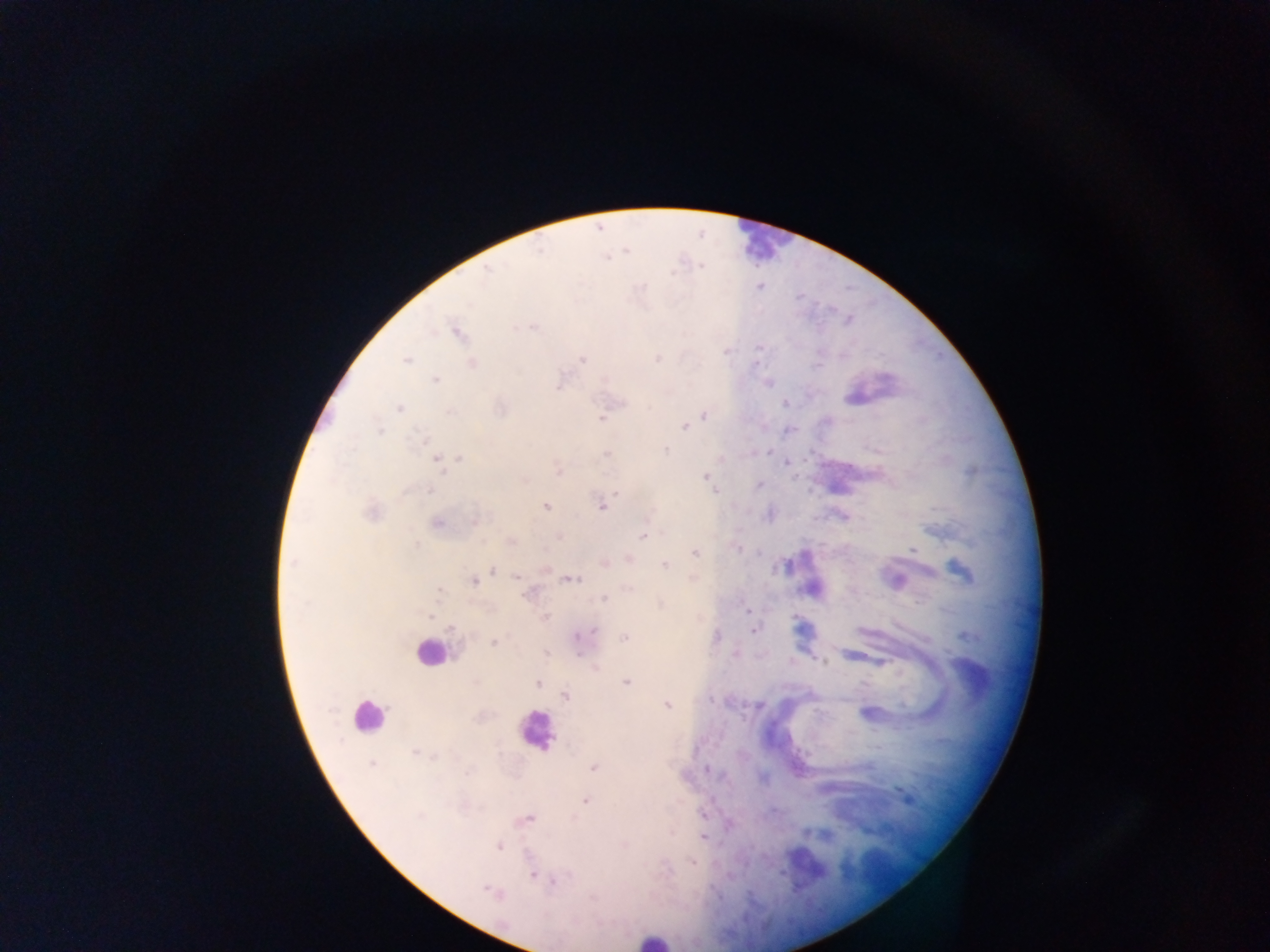

Approximate centers as x y in pixels. Malaria parasite locations: 488 269; 760 286; 532 327; 458 333; 759 347; 658 358; 406 359; 582 359; 473 363; 436 380; 768 384; 558 387; 785 403; 399 409; 450 411; 704 415; 601 419; 685 427; 380 430; 423 440; 666 450; 607 453; 460 458; 438 461; 787 462; 559 472; 706 476; 758 485; 430 492; 616 493; 602 506; 545 507; 371 513; 476 521; 438 524; 643 536; 913 549; 695 553; 293 563; 605 563; 665 564; 960 570; 493 571; 516 577; 571 579; 474 581; 439 590; 603 599; 747 611; 544 617; 593 630; 754 631; 625 637; 494 642; 823 663; 539 683; 626 683; 566 697; 667 705; 415 752; 372 764; 594 768; 707 770; 586 801; 528 819; 703 838; 498 846; 692 862; 533 874; 553 883; 490 891. Leukocyte locations: 429 651; 972 678; 366 716; 537 731; 652 939. Image is 1270×952 pixels. One field of view. Thick blood film. Sample from Ghana. Photographed through a microscope with a mobile-phone camera.